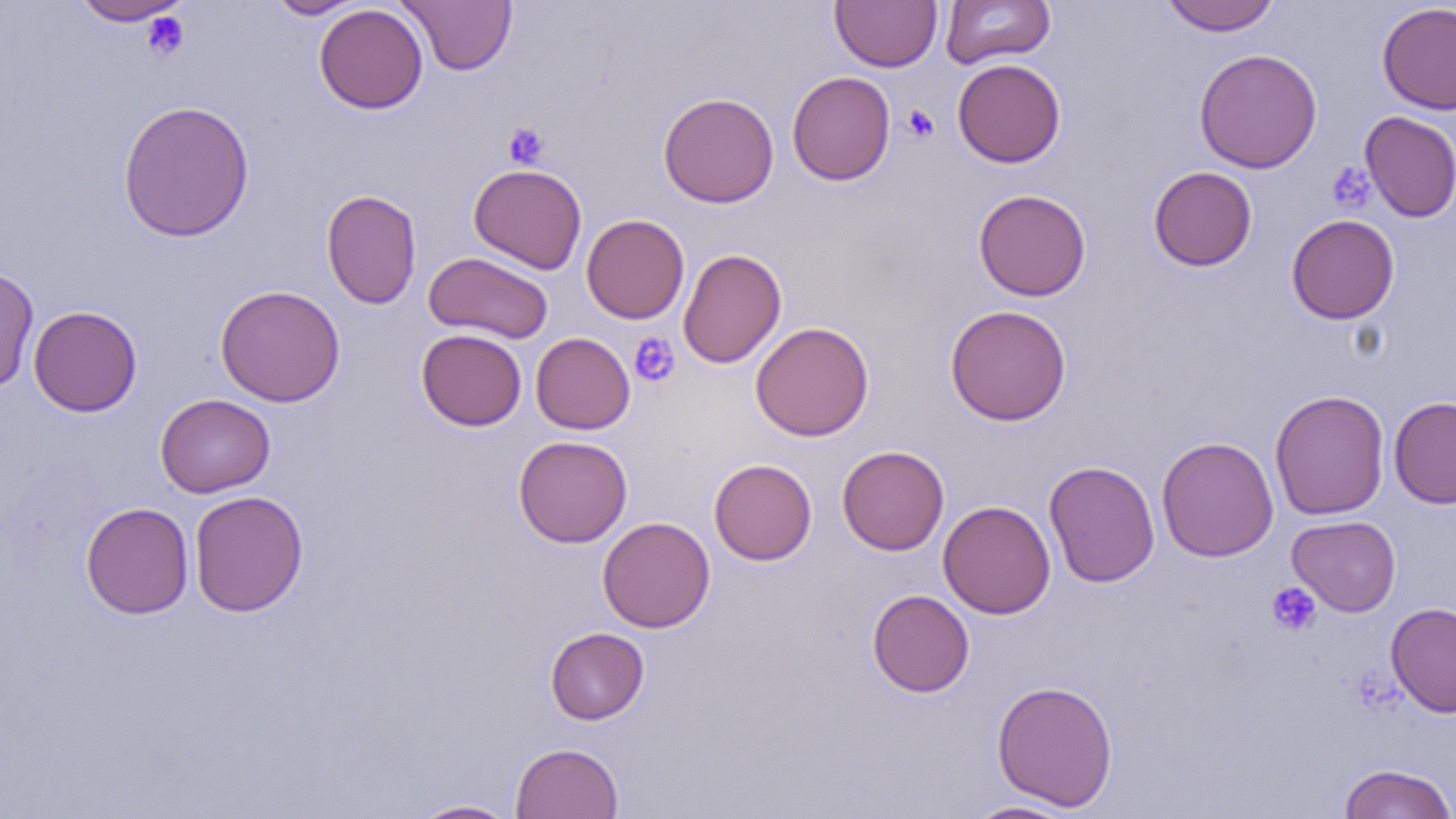 Approximate bounding boxes as named x1/y1/x2/y2 corners in pixels. Platelet locations: (x1=141, y1=12, x2=189, y2=60), (x1=902, y1=104, x2=939, y2=142), (x1=502, y1=121, x2=549, y2=169), (x1=1326, y1=161, x2=1375, y2=213), (x1=628, y1=332, x2=680, y2=387), (x1=1266, y1=582, x2=1321, y2=636). Uninfected red blood cell locations: (x1=70, y1=0, x2=192, y2=26), (x1=265, y1=0, x2=367, y2=19), (x1=399, y1=0, x2=517, y2=75), (x1=831, y1=0, x2=942, y2=72), (x1=941, y1=0, x2=1055, y2=69), (x1=1159, y1=0, x2=1282, y2=36), (x1=1376, y1=2, x2=1456, y2=116), (x1=314, y1=4, x2=428, y2=114), (x1=1194, y1=48, x2=1322, y2=174), (x1=952, y1=58, x2=1066, y2=168), (x1=787, y1=71, x2=895, y2=185), (x1=658, y1=92, x2=779, y2=208), (x1=117, y1=99, x2=255, y2=242), (x1=1360, y1=111, x2=1456, y2=223), (x1=468, y1=163, x2=587, y2=274), (x1=1148, y1=166, x2=1257, y2=271), (x1=321, y1=189, x2=422, y2=309), (x1=973, y1=189, x2=1091, y2=301), (x1=581, y1=214, x2=690, y2=324), (x1=1286, y1=214, x2=1399, y2=324), (x1=678, y1=249, x2=786, y2=369), (x1=424, y1=252, x2=553, y2=344), (x1=0, y1=266, x2=39, y2=393), (x1=215, y1=284, x2=346, y2=407), (x1=945, y1=304, x2=1072, y2=426), (x1=28, y1=305, x2=142, y2=417), (x1=750, y1=322, x2=874, y2=441), (x1=416, y1=328, x2=527, y2=431), (x1=531, y1=332, x2=635, y2=434), (x1=1270, y1=389, x2=1390, y2=521), (x1=155, y1=394, x2=275, y2=498), (x1=1388, y1=396, x2=1456, y2=508), (x1=513, y1=435, x2=632, y2=548), (x1=1156, y1=437, x2=1279, y2=562), (x1=837, y1=445, x2=949, y2=555), (x1=709, y1=459, x2=817, y2=565), (x1=1043, y1=459, x2=1160, y2=588), (x1=189, y1=490, x2=308, y2=617), (x1=938, y1=501, x2=1055, y2=619), (x1=80, y1=502, x2=194, y2=618), (x1=1287, y1=515, x2=1401, y2=616), (x1=598, y1=516, x2=715, y2=633), (x1=867, y1=589, x2=975, y2=697), (x1=1386, y1=602, x2=1456, y2=718), (x1=545, y1=627, x2=648, y2=724), (x1=992, y1=679, x2=1118, y2=811), (x1=510, y1=742, x2=624, y2=819), (x1=1337, y1=763, x2=1456, y2=819), (x1=408, y1=799, x2=519, y2=818), (x1=961, y1=799, x2=1081, y2=818). Slide-level diagnosis: negative for blood parasites. Thin blood smear. Image is 1456×819 pixels. One field of a larger specimen. Optical microscopy. Captured at 1000x magnification.